Locate every Plasmodium falciparum-infected red blood cell.
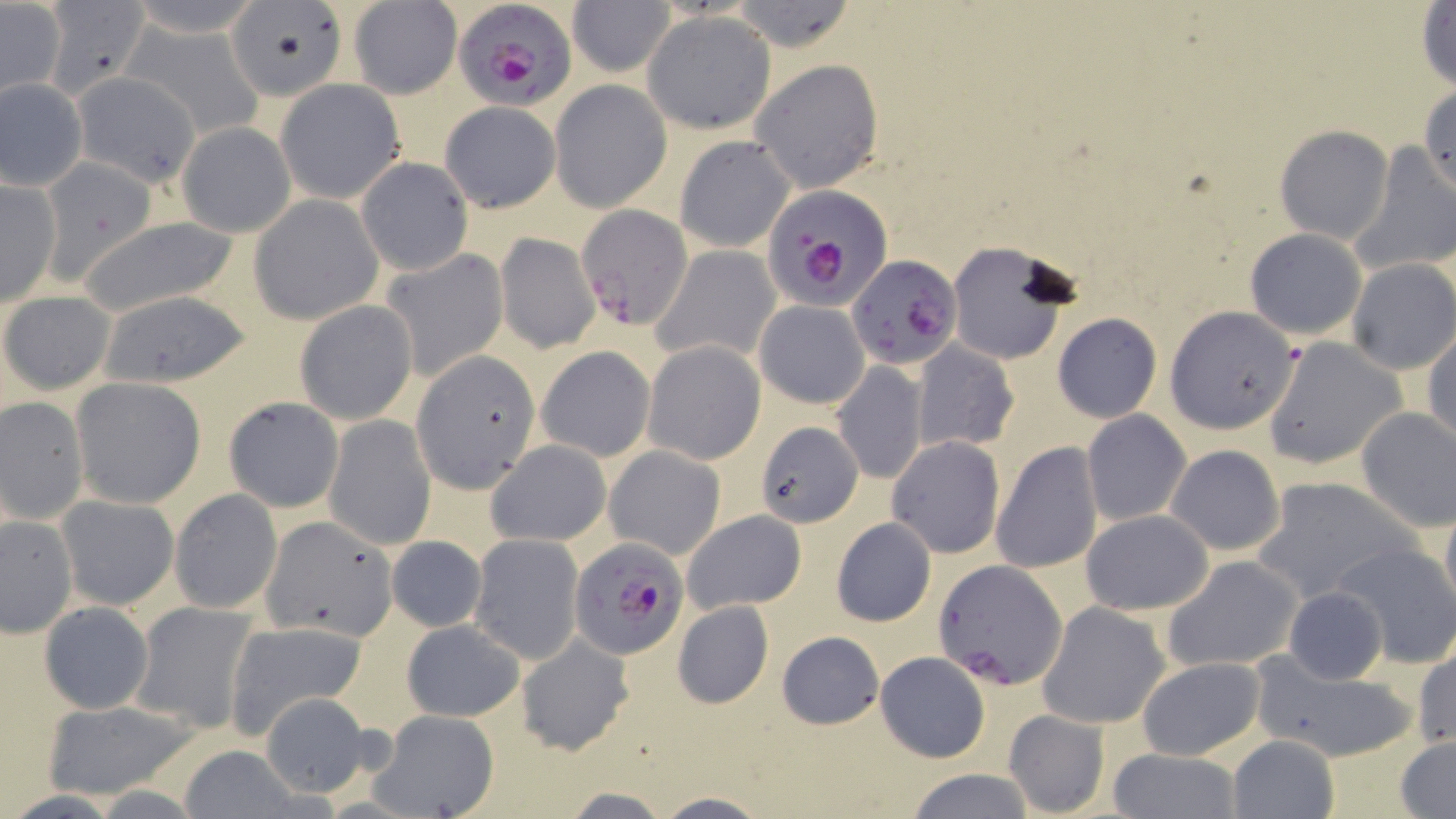
Approximate bounding boxes as (x1,y1)-(x2,y2) corner pairs in pixels.
Plasmodium falciparum-infected red blood cells: (451,0)-(576,111), (759,182)-(891,311), (576,203)-(692,330), (846,254)-(964,368), (570,537)-(688,659), (934,560)-(1068,687).

Summary:
  - Uninfected red blood cell locations: (121,0)-(268,37), (227,0)-(347,101), (724,0)-(861,52), (567,1)-(676,77), (37,2)-(150,100), (1416,3)-(1455,91), (0,4)-(65,99), (349,4)-(459,100), (644,13)-(775,133), (121,24)-(266,135), (750,59)-(884,193), (71,72)-(202,188), (0,77)-(87,191), (276,79)-(406,203), (551,79)-(671,211), (1416,81)-(1456,200), (439,102)-(560,211), (176,122)-(295,237), (1273,125)-(1394,245), (674,135)-(796,253), (1350,147)-(1456,274), (39,156)-(157,285), (355,157)-(473,275), (0,177)-(61,307), (250,196)-(384,325), (74,217)-(243,321), (1244,229)-(1367,341), (495,234)-(600,354), (947,240)-(1079,367), (652,246)-(782,368), (377,248)-(508,383), (1346,258)-(1456,376), (95,291)-(250,388), (1,292)-(116,395), (754,300)-(869,409), (295,301)-(419,425), (1166,305)-(1303,432), (1052,312)-(1162,422), (1424,328)-(1456,451), (1261,337)-(1410,470), (643,341)-(765,464), (912,341)-(1019,454), (535,345)-(655,461), (417,356)-(540,491), (832,361)-(927,486), (68,377)-(206,507), (1,395)-(89,524), (223,396)-(344,512), (1354,407)-(1456,532), (1081,410)-(1191,527), (325,414)-(436,550), (756,421)-(862,525), (887,435)-(1005,559), (485,438)-(612,547), (991,441)-(1103,573), (1165,444)-(1285,557), (605,446)-(725,560), (1250,476)-(1418,606), (170,488)-(282,613), (56,495)-(179,610), (1440,500)-(1456,616), (1080,509)-(1215,615), (682,510)-(807,613), (1,515)-(77,637), (261,517)-(398,641), (830,518)-(937,627), (387,534)-(488,633), (468,534)-(584,663), (1330,540)-(1456,669), (1161,555)-(1303,673), (1282,586)-(1390,685), (38,600)-(154,714), (130,601)-(260,731), (672,601)-(774,709), (1038,602)-(1170,728), (399,619)-(524,722), (224,621)-(369,735), (777,630)-(884,727), (515,633)-(635,755), (1413,648)-(1455,750), (1248,652)-(1420,760), (878,654)-(994,765), (1135,656)-(1268,760), (258,691)-(374,796), (36,698)-(201,799), (370,709)-(500,819), (1002,709)-(1111,817), (1227,735)-(1341,819), (1395,736)-(1456,817), (175,746)-(302,816), (1106,749)-(1241,819), (903,767)-(1035,819), (649,793)-(773,818)
  - Slide-level diagnosis: Plasmodium falciparum
  - Field of view: one of a larger specimen
  - Stain: May-Grünwald-Giemsa
  - Modality: light microscopy
  - Magnification: 1000x
  - Image size: 1456×819 pixels
  - Preparation: thin blood smear